Give the extent of all Plasmodium falciparum-infected red blood cells.
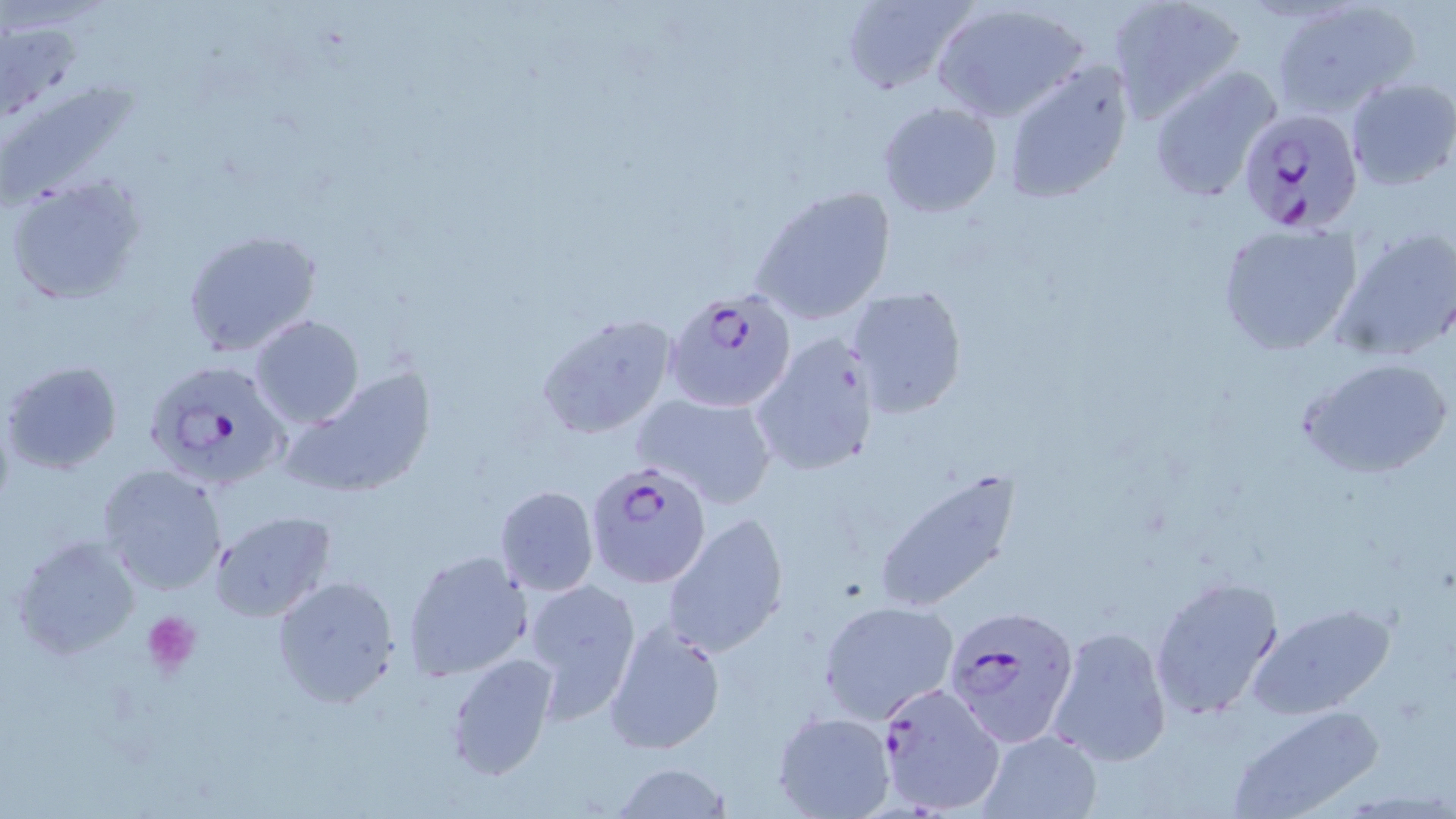

Approximate bounding boxes as (x1, y1, x2, y2) in pixels.
Plasmodium falciparum-infected red blood cells: (1237, 109, 1365, 235), (665, 287, 795, 413), (141, 355, 295, 491), (586, 462, 711, 587), (945, 606, 1078, 748), (872, 679, 1005, 816).

Summary:
  - Platelet locations: (143, 611, 202, 674)
  - Uninfected red blood cell locations: (1104, 0, 1245, 123), (834, 1, 975, 94), (1268, 1, 1420, 117), (931, 3, 1088, 124), (4, 24, 80, 118), (1002, 58, 1136, 206), (1148, 65, 1282, 203), (3, 67, 155, 214), (1344, 76, 1456, 193), (877, 100, 1003, 219), (5, 173, 149, 305), (751, 184, 898, 325), (1217, 222, 1363, 358), (178, 223, 323, 354), (1332, 227, 1456, 362), (845, 285, 968, 417), (535, 313, 679, 440), (250, 315, 363, 428), (751, 329, 883, 478), (1299, 354, 1454, 482), (2, 359, 123, 474), (285, 369, 439, 500), (631, 392, 779, 507), (97, 463, 229, 596), (871, 468, 1024, 612), (493, 484, 599, 595), (210, 510, 335, 624), (661, 511, 791, 657), (10, 532, 143, 660), (402, 549, 533, 682), (271, 574, 399, 707), (1148, 575, 1285, 719), (523, 577, 643, 719), (818, 600, 959, 722), (1249, 603, 1396, 719), (604, 616, 727, 757), (1048, 625, 1173, 767), (444, 652, 557, 779), (1227, 705, 1382, 819), (771, 711, 894, 819), (977, 728, 1100, 817), (609, 761, 732, 818)
  - Slide-level diagnosis: Plasmodium falciparum
  - Field of view: one of a larger specimen
  - Stain: May-Grünwald-Giemsa
  - Modality: optical microscopy
  - Image size: 1456×819 pixels
  - Magnification: 1000x
  - Preparation: thin blood film